Name the blood parasite species.
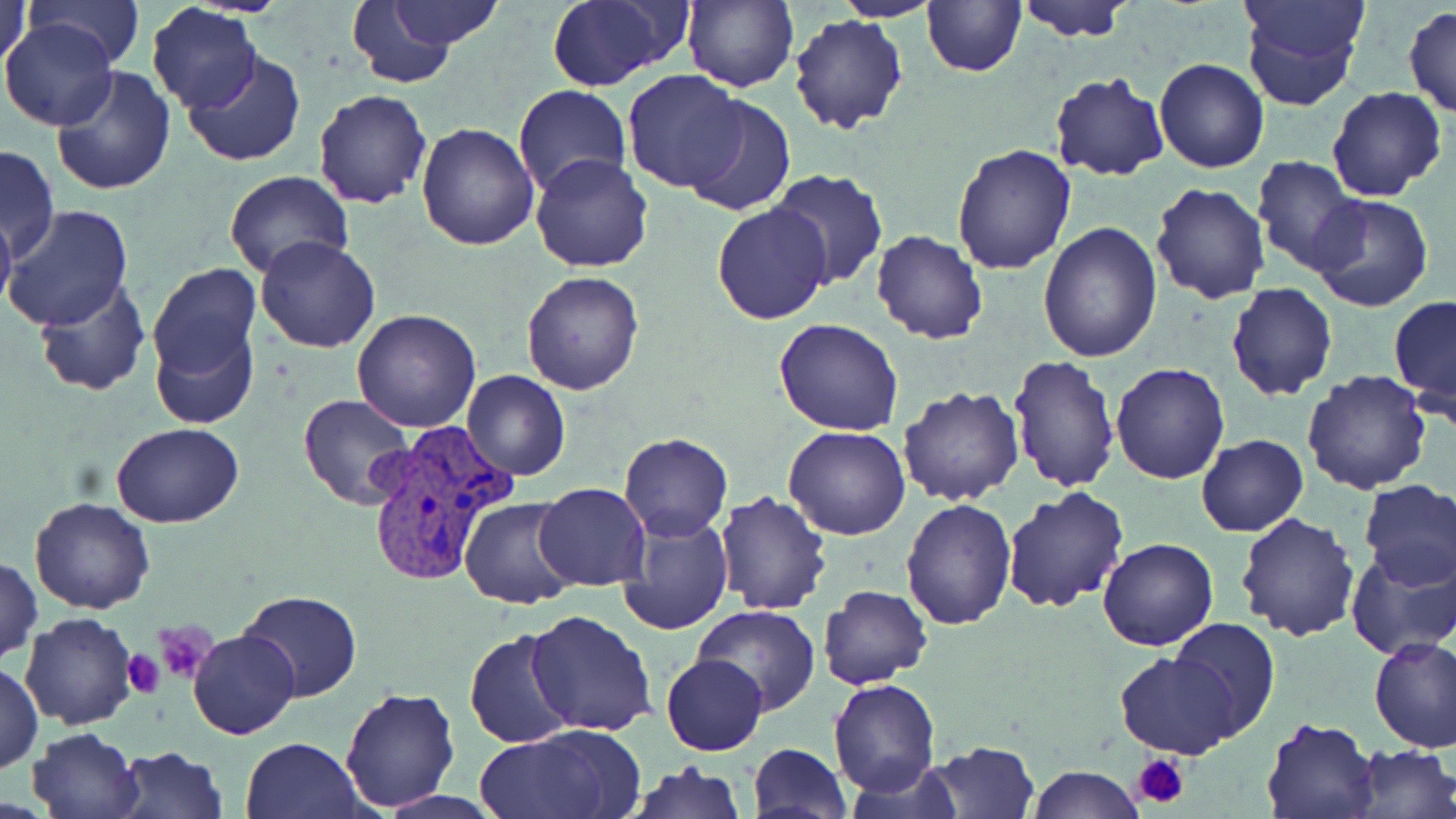
Plasmodium vivax.

Summary:
  - Coordinate format: approximate bounding boxes as (x1, y1, x2, y2) in pixels
  - Platelet locations: (154, 621, 217, 685), (120, 651, 164, 698), (1132, 753, 1188, 809)
  - Plasmodium vivax-infected red blood cell locations: (363, 426, 513, 588)
  - Uninfected red blood cell locations: (0, 0, 31, 83), (25, 0, 143, 67), (682, 0, 798, 93), (834, 0, 942, 23), (921, 0, 1026, 77), (1015, 0, 1134, 43), (1236, 0, 1366, 112), (343, 1, 476, 87), (379, 1, 504, 51), (545, 1, 688, 90), (146, 4, 262, 114), (1403, 6, 1456, 118), (788, 13, 907, 134), (1, 18, 119, 132), (183, 52, 308, 168), (1154, 56, 1269, 173), (51, 65, 177, 197), (622, 69, 750, 194), (1047, 71, 1170, 182), (513, 85, 633, 198), (1327, 86, 1448, 203), (312, 89, 433, 210), (681, 94, 795, 216), (417, 122, 541, 250), (951, 142, 1077, 275), (0, 144, 59, 261), (530, 153, 654, 273), (1252, 154, 1365, 277), (223, 169, 352, 279), (769, 170, 889, 289), (1150, 181, 1271, 303), (1309, 193, 1434, 313), (712, 201, 832, 324), (0, 204, 16, 317), (2, 205, 134, 333), (1038, 221, 1161, 362), (871, 229, 988, 345), (257, 235, 381, 354), (147, 262, 262, 404), (520, 271, 645, 394), (33, 278, 151, 397), (1226, 284, 1338, 401), (1389, 293, 1456, 412), (350, 308, 482, 431), (775, 317, 903, 437), (150, 324, 257, 429), (1007, 352, 1121, 492), (1112, 362, 1229, 483), (1302, 368, 1433, 495), (462, 369, 569, 481), (896, 384, 1024, 505), (298, 395, 415, 510), (110, 422, 242, 529), (784, 426, 910, 541), (618, 431, 733, 541), (1196, 434, 1308, 537), (1357, 480, 1456, 590), (533, 483, 651, 591), (1001, 486, 1130, 613), (713, 490, 833, 613), (459, 495, 581, 609), (28, 497, 155, 614), (901, 497, 1016, 631), (616, 511, 734, 636), (1235, 512, 1362, 643), (1098, 538, 1217, 651), (1343, 543, 1456, 661), (1, 557, 42, 665), (819, 584, 932, 690), (238, 590, 362, 702), (692, 605, 820, 714), (526, 609, 659, 735), (20, 612, 140, 730), (1167, 620, 1280, 741), (187, 628, 300, 740), (465, 628, 577, 748), (1369, 635, 1456, 753), (1116, 650, 1242, 759), (662, 654, 767, 756), (1, 664, 43, 775), (828, 679, 940, 797), (337, 684, 461, 813), (1260, 716, 1382, 819), (28, 726, 144, 819), (474, 727, 639, 819), (241, 737, 366, 819), (923, 740, 1040, 819), (749, 743, 851, 818), (1350, 743, 1455, 819), (113, 744, 228, 818), (627, 760, 746, 818), (840, 762, 960, 817), (1026, 764, 1142, 819)
  - Magnification: 1000x
  - Stain: May-Grünwald-Giemsa
  - Preparation: thin blood film
  - Modality: light microscopy
  - Image size: 1456×819 pixels
  - Field of view: single